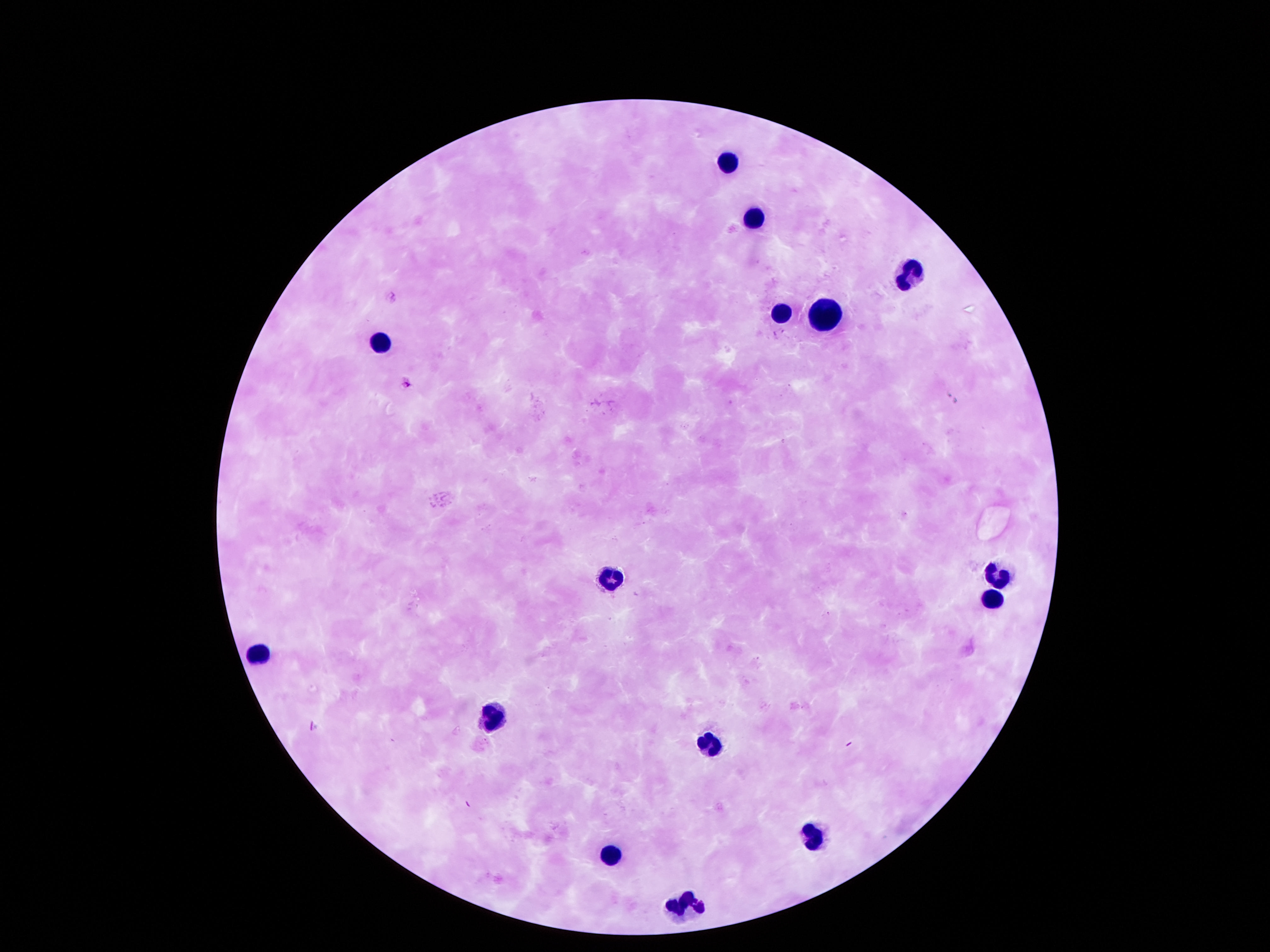
leukocyte locations = approximate object centers, in pixels from the top-left corner: (x=726, y=161), (x=753, y=215), (x=904, y=269), (x=780, y=309), (x=824, y=316), (x=380, y=339), (x=998, y=571), (x=608, y=575), (x=992, y=601), (x=252, y=652), (x=491, y=715), (x=706, y=741), (x=810, y=833), (x=608, y=852), (x=686, y=904)
capture = smartphone camera through the microscope eyepiece
stain = Giemsa
field of view = single
patient malaria status = negative
preparation = thick peripheral-blood smear
magnification = 100x
image size = 1270×952 pixels